Assess the morphology of the erythrocytes.
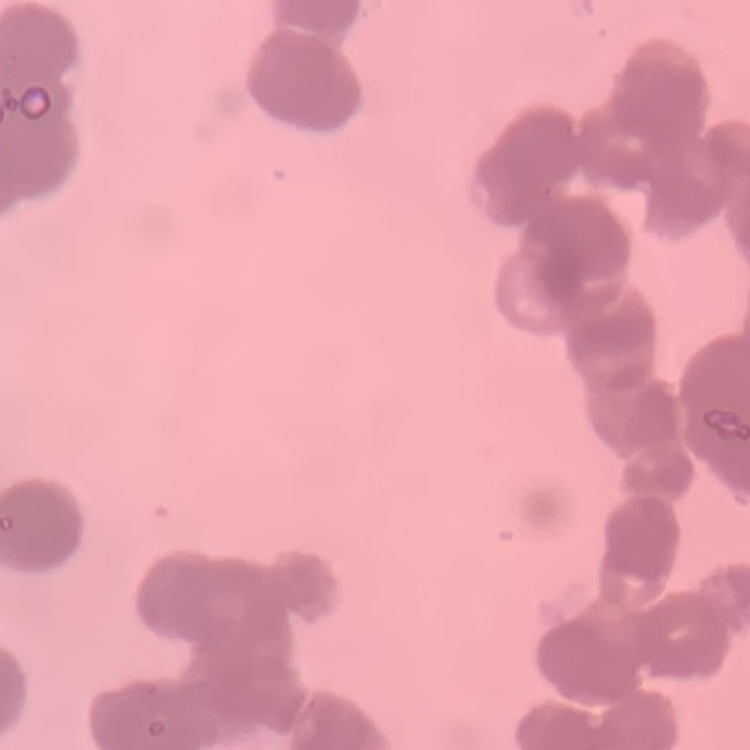
Rouleaux formation.

Thin peripheral smear. Square crop of a larger photomicrograph. Field's or Giemsa stain.